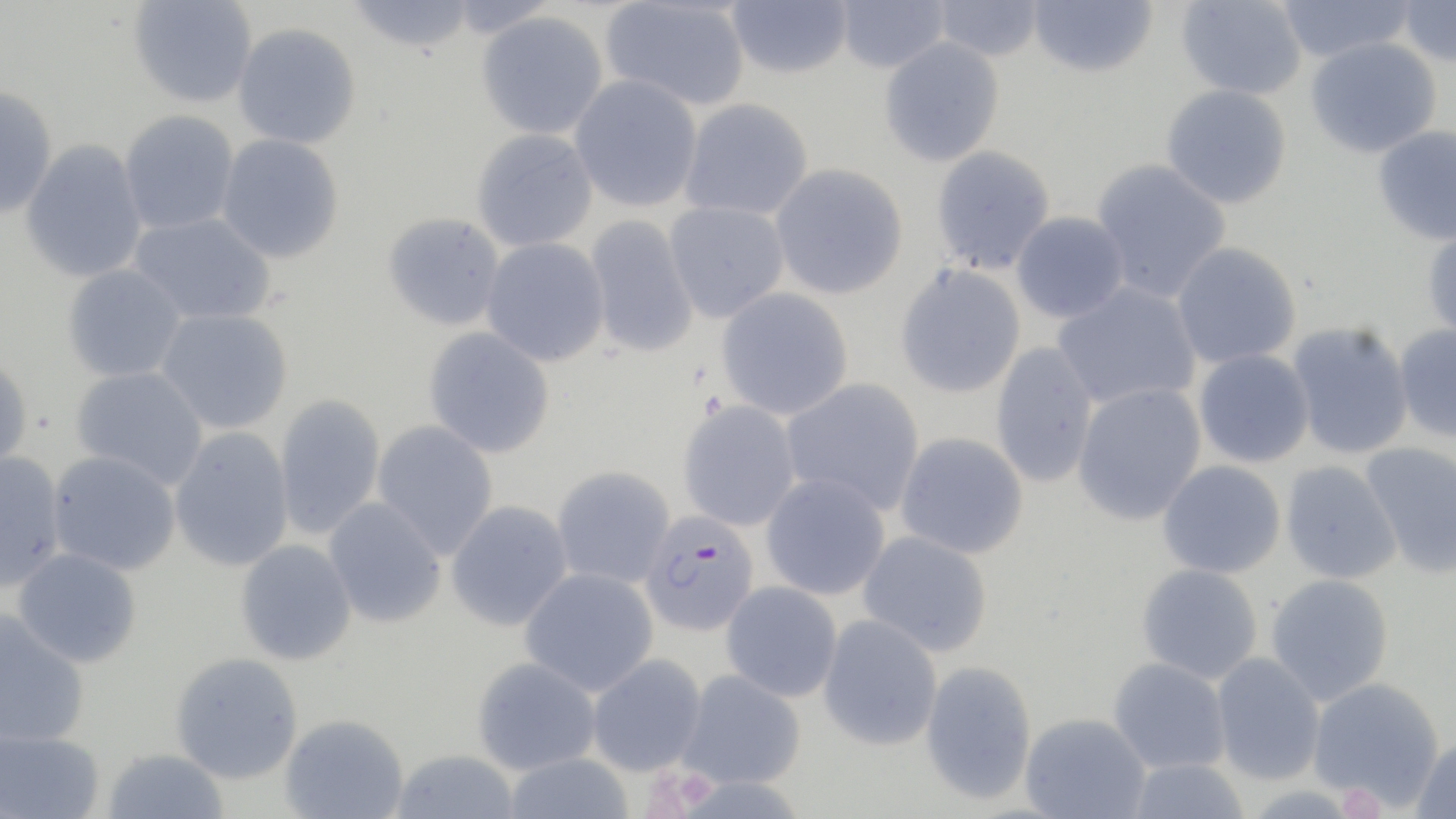
Approximate bounding boxes as named x1/y1/x2/y2 corners in pixels. Plasmodium falciparum-infected red blood cell locations: (x1=640, y1=510, x2=760, y2=636). Uninfected red blood cell locations: (x1=345, y1=0, x2=477, y2=54), (x1=600, y1=0, x2=750, y2=111), (x1=725, y1=0, x2=853, y2=79), (x1=834, y1=0, x2=951, y2=74), (x1=931, y1=0, x2=1045, y2=62), (x1=1027, y1=0, x2=1158, y2=78), (x1=1174, y1=0, x2=1308, y2=100), (x1=1275, y1=0, x2=1418, y2=64), (x1=1395, y1=0, x2=1456, y2=68), (x1=128, y1=1, x2=257, y2=108), (x1=475, y1=12, x2=609, y2=140), (x1=232, y1=22, x2=361, y2=150), (x1=878, y1=37, x2=1005, y2=167), (x1=1305, y1=37, x2=1442, y2=159), (x1=569, y1=74, x2=703, y2=212), (x1=0, y1=84, x2=58, y2=219), (x1=1161, y1=84, x2=1292, y2=209), (x1=679, y1=98, x2=814, y2=221), (x1=119, y1=110, x2=239, y2=234), (x1=1372, y1=125, x2=1456, y2=246), (x1=470, y1=129, x2=598, y2=252), (x1=216, y1=134, x2=344, y2=264), (x1=20, y1=139, x2=148, y2=283), (x1=930, y1=145, x2=1056, y2=275), (x1=1090, y1=159, x2=1232, y2=304), (x1=770, y1=163, x2=909, y2=300), (x1=663, y1=201, x2=790, y2=323), (x1=1011, y1=211, x2=1130, y2=324), (x1=128, y1=212, x2=276, y2=325), (x1=382, y1=212, x2=505, y2=331), (x1=584, y1=215, x2=699, y2=359), (x1=1422, y1=224, x2=1456, y2=343), (x1=481, y1=238, x2=610, y2=367), (x1=1171, y1=242, x2=1302, y2=369), (x1=62, y1=263, x2=186, y2=382), (x1=894, y1=265, x2=1026, y2=398), (x1=1052, y1=282, x2=1202, y2=411), (x1=716, y1=287, x2=854, y2=420), (x1=155, y1=308, x2=294, y2=434), (x1=1286, y1=322, x2=1414, y2=459), (x1=1393, y1=324, x2=1456, y2=443), (x1=423, y1=326, x2=556, y2=459), (x1=990, y1=343, x2=1099, y2=487), (x1=1193, y1=349, x2=1314, y2=468), (x1=0, y1=354, x2=33, y2=476), (x1=70, y1=366, x2=208, y2=490), (x1=780, y1=377, x2=925, y2=515), (x1=1072, y1=383, x2=1207, y2=525), (x1=274, y1=393, x2=386, y2=540), (x1=677, y1=399, x2=801, y2=532), (x1=371, y1=420, x2=499, y2=559), (x1=169, y1=426, x2=294, y2=572), (x1=895, y1=432, x2=1029, y2=559), (x1=1360, y1=442, x2=1456, y2=579), (x1=46, y1=450, x2=182, y2=575), (x1=0, y1=451, x2=67, y2=592), (x1=1158, y1=460, x2=1286, y2=578), (x1=1280, y1=460, x2=1402, y2=584), (x1=552, y1=466, x2=674, y2=588), (x1=761, y1=473, x2=890, y2=600), (x1=323, y1=498, x2=446, y2=628), (x1=445, y1=500, x2=573, y2=631), (x1=857, y1=530, x2=993, y2=657), (x1=235, y1=539, x2=357, y2=666), (x1=12, y1=548, x2=142, y2=668), (x1=1136, y1=563, x2=1263, y2=684), (x1=519, y1=568, x2=659, y2=696), (x1=1265, y1=573, x2=1394, y2=706), (x1=721, y1=581, x2=842, y2=702), (x1=0, y1=610, x2=89, y2=746), (x1=817, y1=615, x2=942, y2=751), (x1=170, y1=652, x2=304, y2=784), (x1=587, y1=653, x2=707, y2=776), (x1=1211, y1=653, x2=1325, y2=785), (x1=472, y1=657, x2=600, y2=774), (x1=1108, y1=657, x2=1231, y2=774), (x1=920, y1=660, x2=1037, y2=805), (x1=676, y1=670, x2=806, y2=789), (x1=1307, y1=677, x2=1445, y2=809), (x1=1019, y1=713, x2=1151, y2=819), (x1=279, y1=714, x2=409, y2=819), (x1=0, y1=727, x2=105, y2=819), (x1=1411, y1=737, x2=1456, y2=819), (x1=102, y1=747, x2=229, y2=819), (x1=389, y1=749, x2=520, y2=819), (x1=502, y1=752, x2=635, y2=819), (x1=1126, y1=757, x2=1251, y2=819). Platelet locations: (x1=1337, y1=784, x2=1385, y2=818). Slide-level diagnosis: Plasmodium falciparum. Image is 1456×819 pixels. Thin blood film. Optical microscopy. Captured at 1000x magnification. May-Grünwald-Giemsa stain. Single field of view.